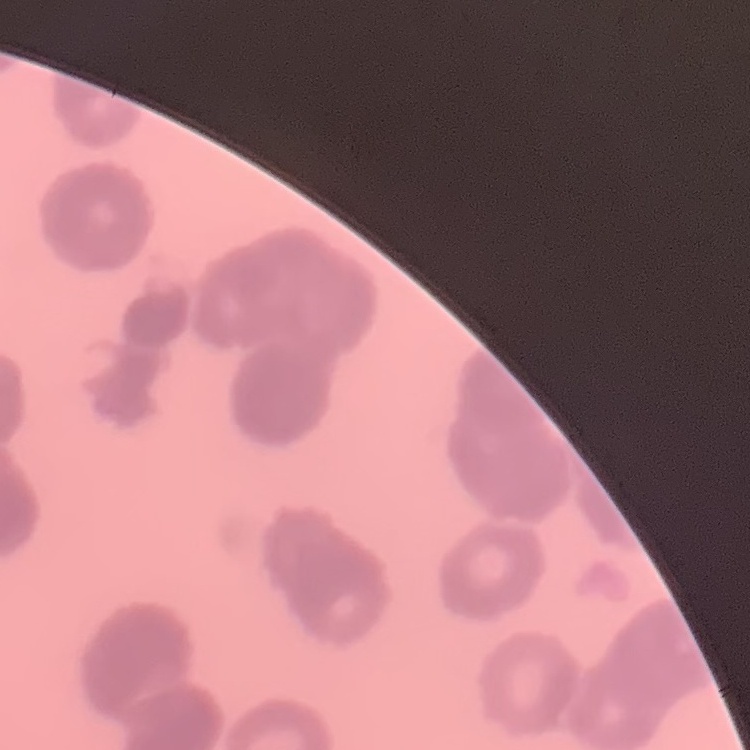
{
  "red_blood_cell_morphology": "rouleaux formation",
  "stain": "Field's or Giemsa",
  "image_type": "square crop of a larger photomicrograph",
  "preparation": "thin blood smear"
}